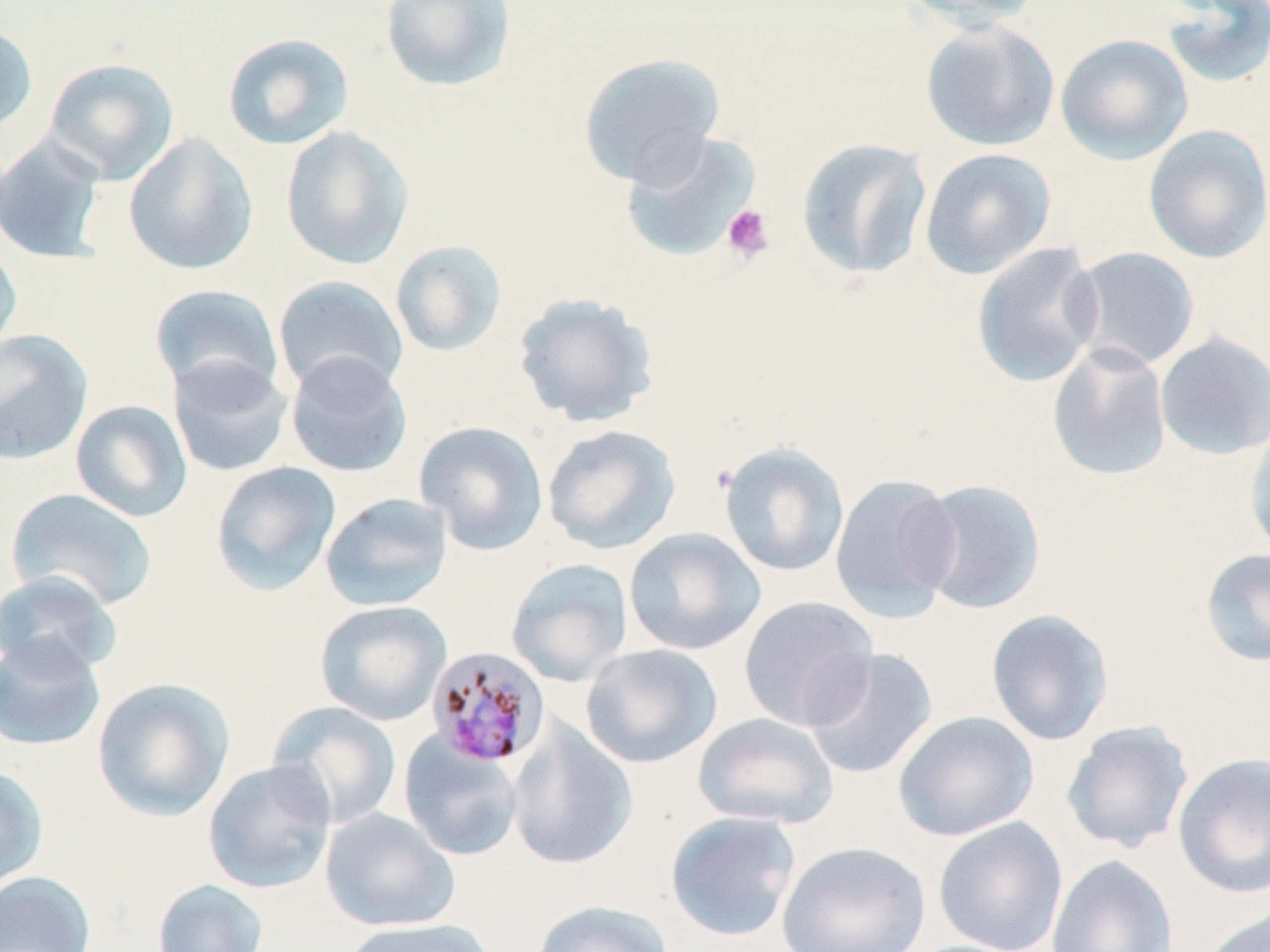
Summary:
  - Coordinate format: approximate bounding boxes as (x1,y1)-(x2,y2) corner pairs in pixels
  - Uninfected red blood cell locations: (380,0)-(517,93), (898,0)-(1046,29), (1161,1)-(1270,90), (920,20)-(1059,151), (0,22)-(39,134), (222,32)-(355,151), (1055,34)-(1193,165), (578,52)-(725,187), (43,57)-(180,184), (1143,124)-(1270,264), (280,125)-(414,269), (617,129)-(762,264), (123,132)-(258,275), (0,133)-(109,265), (796,138)-(932,281), (919,148)-(1056,279), (0,239)-(23,358), (389,240)-(508,357), (971,241)-(1104,388), (1067,246)-(1201,372), (272,274)-(409,397), (149,283)-(285,399), (512,292)-(658,428), (0,329)-(93,466), (1154,330)-(1270,461), (1046,342)-(1172,482), (285,352)-(413,478), (167,355)-(294,477), (70,400)-(192,522), (1243,419)-(1270,564), (414,420)-(549,555), (542,423)-(681,554), (719,441)-(850,577), (210,461)-(341,596), (830,474)-(962,622), (912,478)-(1047,614), (5,488)-(159,613), (319,492)-(453,612), (623,527)-(766,655), (1198,548)-(1270,667), (505,558)-(633,687), (0,570)-(123,680), (739,595)-(879,731), (314,600)-(452,726), (985,608)-(1115,746), (0,636)-(106,753), (580,643)-(723,769), (802,647)-(939,780), (91,677)-(235,822), (267,701)-(402,830), (893,710)-(1039,841), (693,712)-(840,830), (506,719)-(638,871), (1061,720)-(1195,854), (398,732)-(526,862), (1172,752)-(1270,899), (202,759)-(336,894), (0,765)-(49,892), (320,806)-(460,932), (665,810)-(802,942), (933,816)-(1069,952), (776,840)-(931,952), (1046,854)-(1178,952), (0,870)-(96,952), (151,879)-(270,952), (530,898)-(675,952), (1198,902)-(1270,952), (340,917)-(497,952)
  - Plasmodium malariae-infected red blood cell locations: (425,646)-(551,769)
  - Platelet locations: (721,204)-(774,262)
  - Slide-level diagnosis: Plasmodium malariae
  - Magnification: 1000x
  - Field of view: one of a larger specimen
  - Modality: optical microscopy
  - Stain: May-Grünwald-Giemsa
  - Preparation: thin blood film
  - Image size: 1270×952 pixels